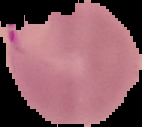
result = Plasmodium parasites detected
preparation = thin blood film
image type = segmented cell region with the area outside set to black
image size = 142×127 pixels